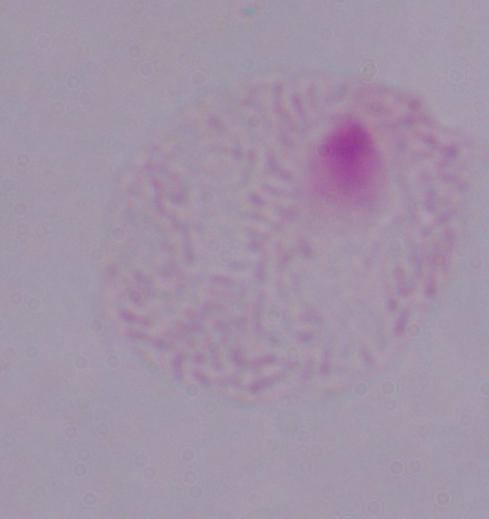
modality = photomicrograph
identification = trichomonad
magnification = 1000x